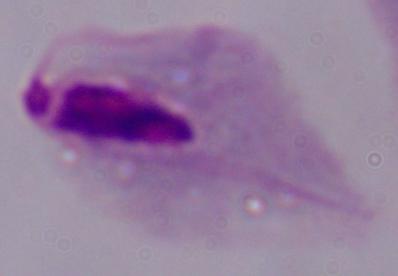
magnification = 1000x
modality = photomicrograph
identification = trichomonad